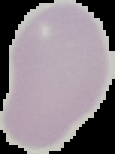

image size = 115×154 pixels
malaria status = uninfected
image type = cell region segmented out of the field of view; surrounding area masked to black
preparation = thin blood smear